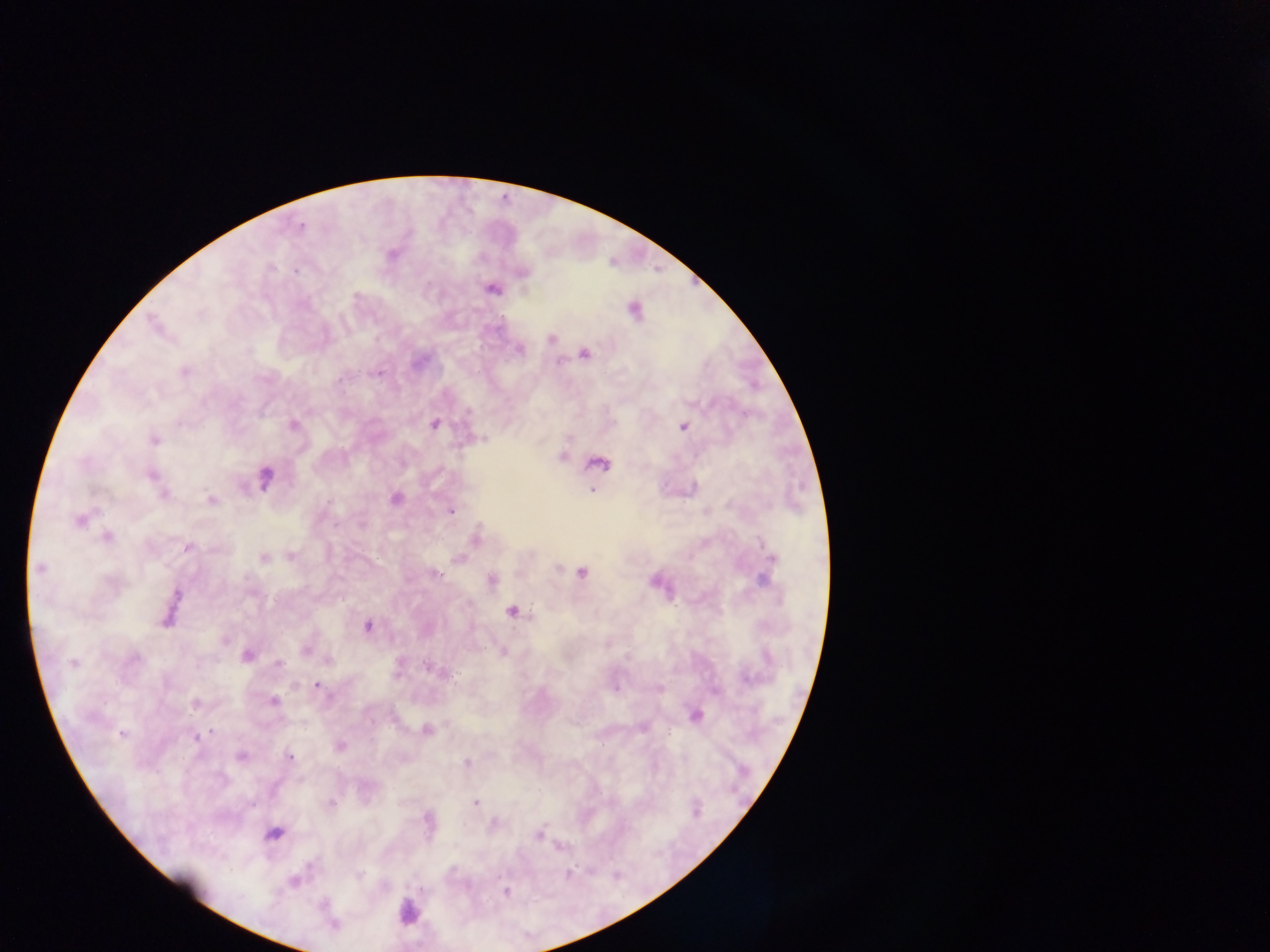

Approximate centers as [x, y] in pixels. Leukocyte locations: [407, 912]. Malaria parasite locations: [300, 227], [390, 254], [522, 272], [491, 289], [634, 310], [156, 326], [551, 338], [519, 349], [584, 352], [185, 371], [434, 423], [292, 425], [683, 426], [153, 439], [561, 455], [598, 464], [151, 475], [264, 478], [592, 489], [159, 492], [395, 499], [210, 500], [450, 511], [80, 519], [107, 536], [475, 538], [186, 548], [291, 556], [264, 557], [458, 558], [770, 561], [39, 569], [436, 573], [581, 573], [490, 580], [657, 582], [169, 609], [511, 612], [367, 626], [224, 637], [307, 649], [503, 651], [246, 654], [327, 660], [73, 663], [278, 663], [440, 673], [317, 686], [659, 688], [273, 701], [195, 704], [694, 716], [426, 730], [123, 734], [197, 737], [339, 747], [240, 756], [289, 757], [466, 762], [475, 803], [331, 804], [427, 821], [493, 823], [273, 834], [538, 834], [294, 881], [505, 890], [333, 925]. Thick blood film. Mobile-phone photograph taken through the microscope. Sample from Ghana. Image is 1270×952 pixels. One field of view.